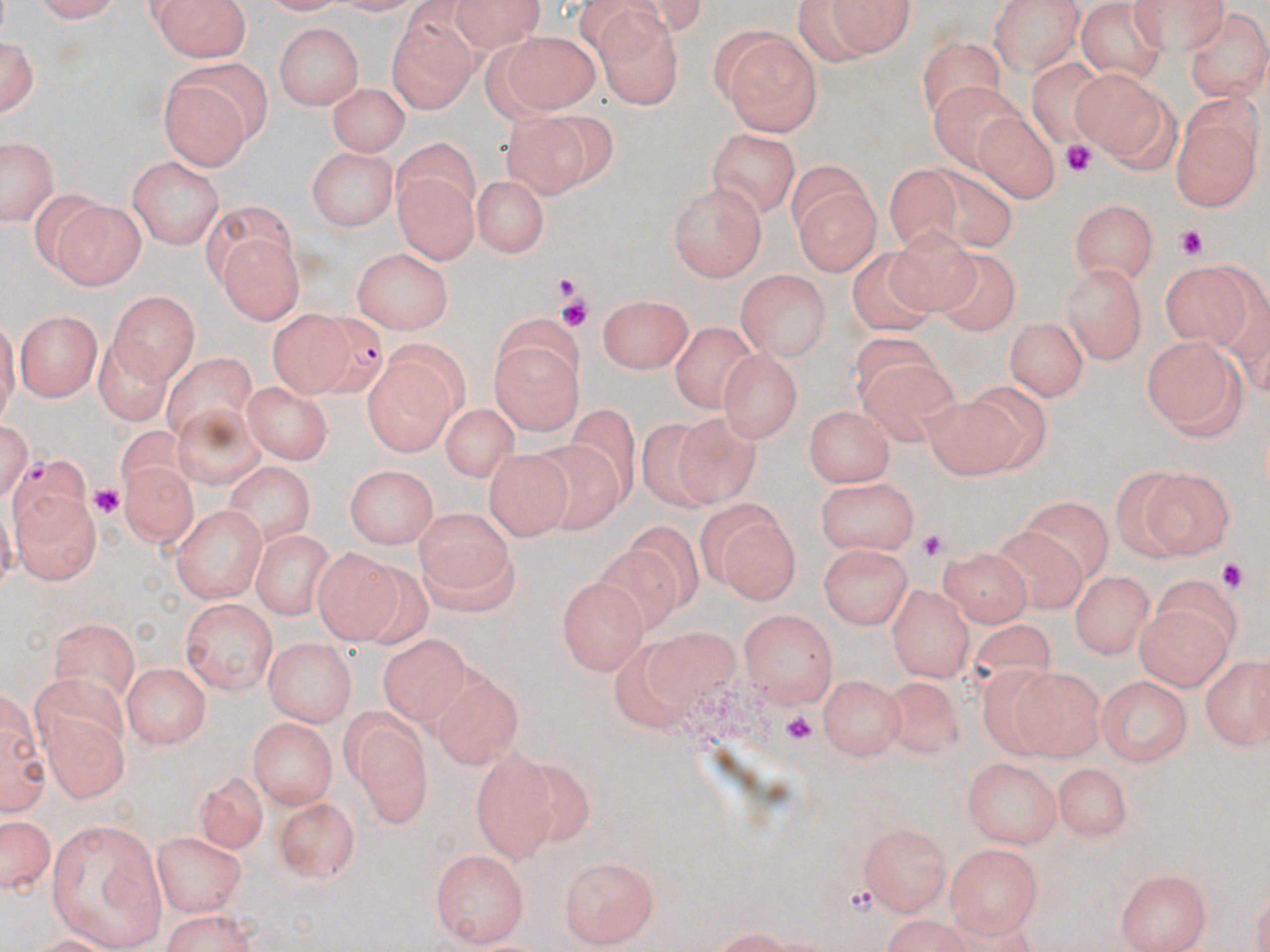

Approximate bounding boxes as named x1/y1/x2/y2 corners in pixels. Platelet locations: (x1=1060, y1=143, x2=1095, y2=173), (x1=1177, y1=224, x2=1212, y2=259), (x1=553, y1=275, x2=581, y2=295), (x1=559, y1=297, x2=588, y2=327), (x1=89, y1=481, x2=126, y2=516), (x1=917, y1=526, x2=944, y2=562), (x1=1209, y1=559, x2=1251, y2=591), (x1=779, y1=713, x2=817, y2=745). Uninfected red blood cell locations: (x1=32, y1=0, x2=131, y2=24), (x1=149, y1=0, x2=251, y2=62), (x1=445, y1=0, x2=547, y2=46), (x1=983, y1=0, x2=1084, y2=75), (x1=1126, y1=0, x2=1229, y2=48), (x1=796, y1=1, x2=917, y2=65), (x1=1076, y1=5, x2=1170, y2=84), (x1=386, y1=7, x2=475, y2=109), (x1=1186, y1=10, x2=1269, y2=100), (x1=593, y1=14, x2=686, y2=108), (x1=274, y1=24, x2=365, y2=112), (x1=722, y1=30, x2=822, y2=133), (x1=0, y1=31, x2=39, y2=118), (x1=495, y1=31, x2=599, y2=117), (x1=915, y1=41, x2=1003, y2=120), (x1=1027, y1=55, x2=1119, y2=147), (x1=156, y1=66, x2=263, y2=171), (x1=1074, y1=69, x2=1177, y2=168), (x1=326, y1=81, x2=409, y2=159), (x1=931, y1=81, x2=1028, y2=175), (x1=1171, y1=101, x2=1263, y2=211), (x1=507, y1=107, x2=608, y2=194), (x1=973, y1=110, x2=1058, y2=205), (x1=705, y1=130, x2=802, y2=218), (x1=3, y1=141, x2=55, y2=223), (x1=308, y1=148, x2=398, y2=232), (x1=395, y1=151, x2=475, y2=258), (x1=128, y1=157, x2=224, y2=248), (x1=920, y1=160, x2=1023, y2=253), (x1=888, y1=163, x2=960, y2=255), (x1=787, y1=172, x2=879, y2=275), (x1=469, y1=173, x2=550, y2=255), (x1=670, y1=184, x2=767, y2=280), (x1=52, y1=198, x2=145, y2=288), (x1=1069, y1=198, x2=1157, y2=282), (x1=197, y1=202, x2=297, y2=282), (x1=884, y1=225, x2=984, y2=316), (x1=218, y1=234, x2=302, y2=326), (x1=851, y1=246, x2=937, y2=334), (x1=354, y1=248, x2=453, y2=333), (x1=936, y1=252, x2=1024, y2=337), (x1=1162, y1=259, x2=1258, y2=345), (x1=1063, y1=262, x2=1150, y2=363), (x1=734, y1=269, x2=832, y2=362), (x1=109, y1=288, x2=198, y2=380), (x1=599, y1=294, x2=694, y2=375), (x1=15, y1=307, x2=104, y2=400), (x1=267, y1=309, x2=351, y2=401), (x1=492, y1=319, x2=584, y2=436), (x1=1005, y1=319, x2=1084, y2=402), (x1=671, y1=320, x2=759, y2=413), (x1=840, y1=328, x2=940, y2=403), (x1=98, y1=335, x2=174, y2=429), (x1=1140, y1=335, x2=1245, y2=442), (x1=718, y1=349, x2=800, y2=443), (x1=160, y1=350, x2=258, y2=435), (x1=857, y1=360, x2=962, y2=450), (x1=362, y1=364, x2=460, y2=456), (x1=242, y1=383, x2=333, y2=463), (x1=922, y1=385, x2=1038, y2=475), (x1=174, y1=396, x2=267, y2=492), (x1=445, y1=399, x2=518, y2=487), (x1=804, y1=402, x2=896, y2=485), (x1=572, y1=407, x2=638, y2=499), (x1=676, y1=412, x2=770, y2=513), (x1=641, y1=415, x2=720, y2=515), (x1=117, y1=422, x2=198, y2=498), (x1=534, y1=440, x2=625, y2=539), (x1=485, y1=447, x2=573, y2=538), (x1=122, y1=462, x2=200, y2=554), (x1=226, y1=463, x2=315, y2=545), (x1=346, y1=464, x2=439, y2=549), (x1=1107, y1=468, x2=1202, y2=561), (x1=1140, y1=468, x2=1236, y2=560), (x1=817, y1=479, x2=921, y2=557), (x1=12, y1=486, x2=101, y2=585), (x1=1025, y1=495, x2=1118, y2=579), (x1=707, y1=504, x2=801, y2=605), (x1=174, y1=506, x2=266, y2=603), (x1=416, y1=511, x2=511, y2=591), (x1=623, y1=519, x2=708, y2=606), (x1=984, y1=525, x2=1087, y2=618), (x1=249, y1=527, x2=338, y2=618), (x1=414, y1=539, x2=518, y2=621), (x1=820, y1=542, x2=913, y2=630), (x1=594, y1=544, x2=682, y2=635), (x1=312, y1=545, x2=403, y2=643), (x1=942, y1=548, x2=1033, y2=628), (x1=1069, y1=570, x2=1153, y2=656), (x1=556, y1=573, x2=646, y2=674), (x1=887, y1=582, x2=973, y2=682), (x1=179, y1=599, x2=276, y2=695), (x1=1137, y1=602, x2=1229, y2=688), (x1=738, y1=609, x2=839, y2=706), (x1=51, y1=615, x2=142, y2=700), (x1=957, y1=620, x2=1066, y2=706), (x1=645, y1=629, x2=739, y2=700), (x1=378, y1=633, x2=471, y2=726), (x1=262, y1=638, x2=358, y2=722), (x1=614, y1=641, x2=697, y2=731), (x1=1203, y1=658, x2=1267, y2=750), (x1=120, y1=660, x2=213, y2=749), (x1=973, y1=662, x2=1080, y2=761), (x1=1007, y1=667, x2=1104, y2=760), (x1=882, y1=674, x2=969, y2=761), (x1=819, y1=675, x2=905, y2=761), (x1=1096, y1=675, x2=1193, y2=768), (x1=437, y1=679, x2=520, y2=771), (x1=2, y1=689, x2=47, y2=822), (x1=38, y1=704, x2=130, y2=806), (x1=343, y1=712, x2=433, y2=829), (x1=249, y1=716, x2=336, y2=809), (x1=471, y1=753, x2=555, y2=862), (x1=510, y1=758, x2=596, y2=846), (x1=963, y1=758, x2=1060, y2=847), (x1=1050, y1=762, x2=1133, y2=840), (x1=193, y1=770, x2=265, y2=851), (x1=268, y1=797, x2=359, y2=882), (x1=0, y1=811, x2=55, y2=898), (x1=48, y1=819, x2=168, y2=946), (x1=859, y1=822, x2=951, y2=915), (x1=151, y1=829, x2=250, y2=914), (x1=948, y1=842, x2=1043, y2=942), (x1=430, y1=849, x2=531, y2=944), (x1=559, y1=856, x2=660, y2=947), (x1=155, y1=865, x2=254, y2=934), (x1=1117, y1=867, x2=1212, y2=950), (x1=155, y1=910, x2=264, y2=952), (x1=872, y1=917, x2=981, y2=951). Plasmodium falciparum-infected red blood cell locations: (x1=305, y1=311, x2=380, y2=395), (x1=10, y1=451, x2=90, y2=541). Slide-level diagnosis: Plasmodium falciparum. Thin blood smear. May-Grünwald-Giemsa-stained preparation. One field of a larger specimen. Image is 1270×952 pixels. Light microscopy. Captured at 1000x magnification.